Report the malaria status of this cell.
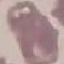

It is uninfected.

Summary:
  - Preparation: thin blood smear
  - Image type: automatically extracted cell patch, resized to 64 × 64 pixels
  - Stain: Giemsa
  - Capture: smartphone through the microscope eyepiece